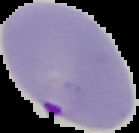
Segmented cell region on a black background. Result: Plasmodium parasites detected. Image is 139×133 pixels. From a thin blood film.